Classify this cell by malaria status.
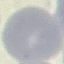

Uninfected.

Thin smear of blood. Photographed with a smartphone camera at the microscope eyepiece. Giemsa stain. Cell patch, automatically extracted from a larger field of view and resized to 64 × 64 pixels.